State the preparation type.
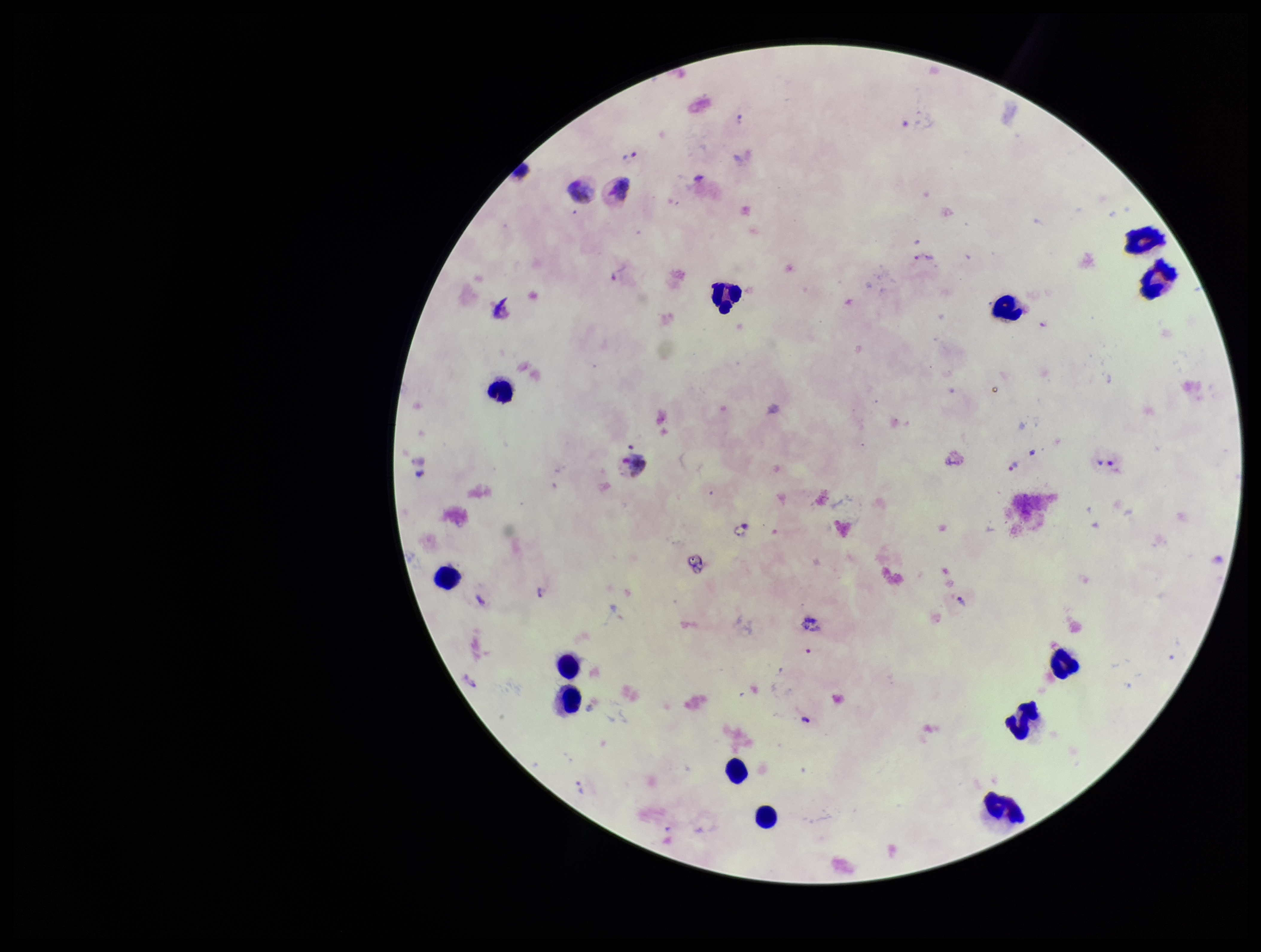

A thick smear.

Parasite count: 9. Giemsa stain. Plasmodium parasites: detected. Species reported for this patient: Plasmodium vivax. Single field of view. Smartphone photograph taken through the eyepiece of a microscope. Leukocyte count: 15. Patient malaria status: positive. Image is 1261×952 pixels.